Locate every blood parasite and identify its species.
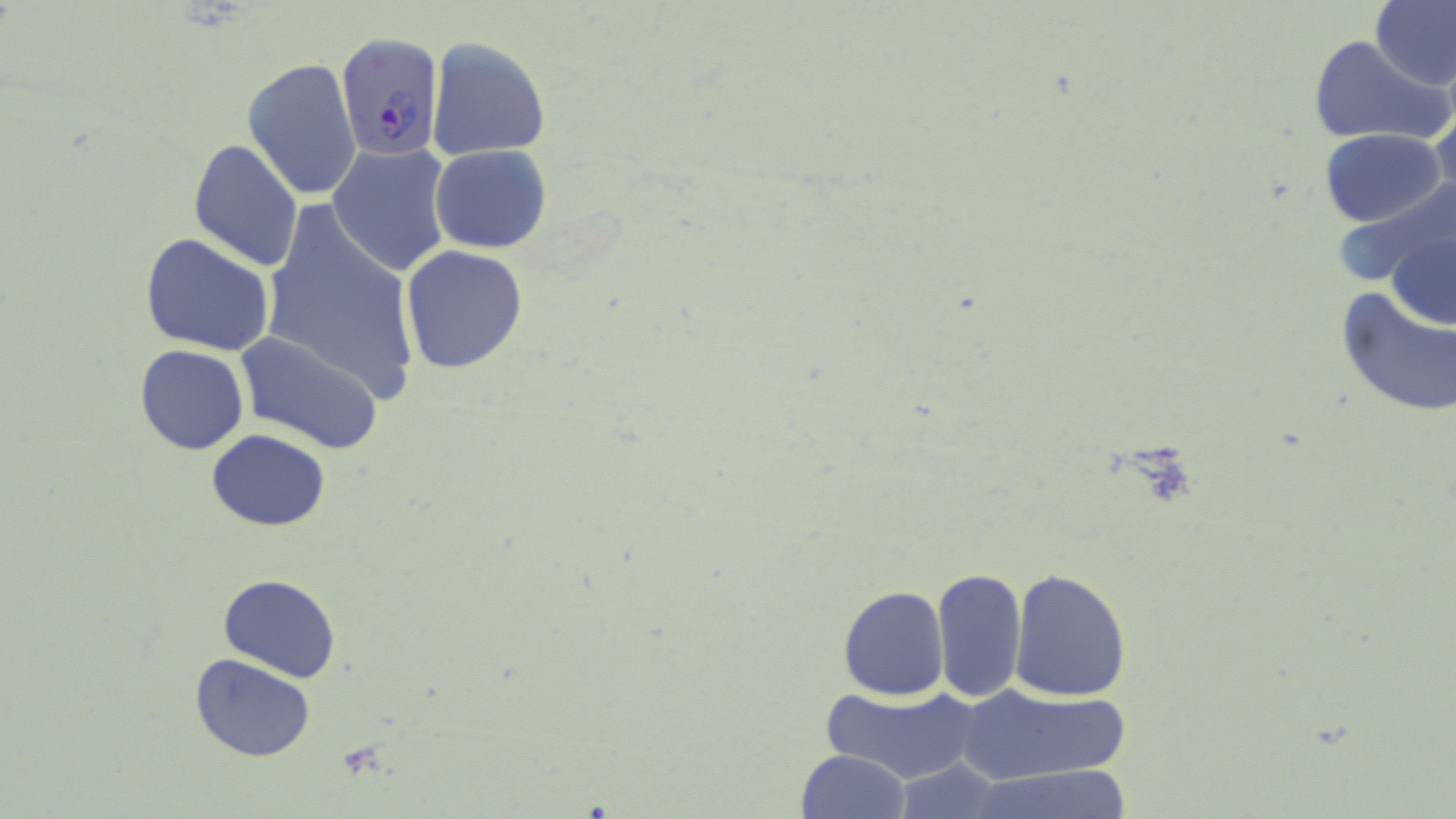

Approximate bounding boxes as (x1,y1)-(x2,y2) corner pairs in pixels.
Plasmodium falciparum-infected red blood cells: (336,32)-(444,162).
No Plasmodium ovale, Plasmodium malariae, Plasmodium vivax, Babesia divergens, or Trypanosoma brucei observed.

Uninfected red blood cell locations: (1372,0)-(1456,90), (1307,35)-(1452,148), (426,36)-(551,163), (243,56)-(362,201), (1431,101)-(1456,201), (1319,128)-(1447,227), (187,138)-(305,272), (327,144)-(454,276), (430,145)-(552,253), (1344,177)-(1456,310), (254,201)-(423,409), (1384,214)-(1455,337), (140,231)-(276,356), (399,246)-(527,374), (1336,287)-(1455,419), (239,332)-(385,454), (135,344)-(249,455), (206,430)-(330,530), (932,567)-(1027,703), (1010,569)-(1130,702), (218,574)-(341,683), (837,585)-(949,701), (189,654)-(317,762), (955,681)-(1135,786), (816,682)-(985,787), (794,749)-(910,819), (894,758)-(1005,818), (967,767)-(1134,819). Slide-level diagnosis: Plasmodium falciparum. Optical microscopy. 1000x magnification. Single field of view. Thin blood smear. May-Grünwald-Giemsa stain. Image is 1456×819 pixels.